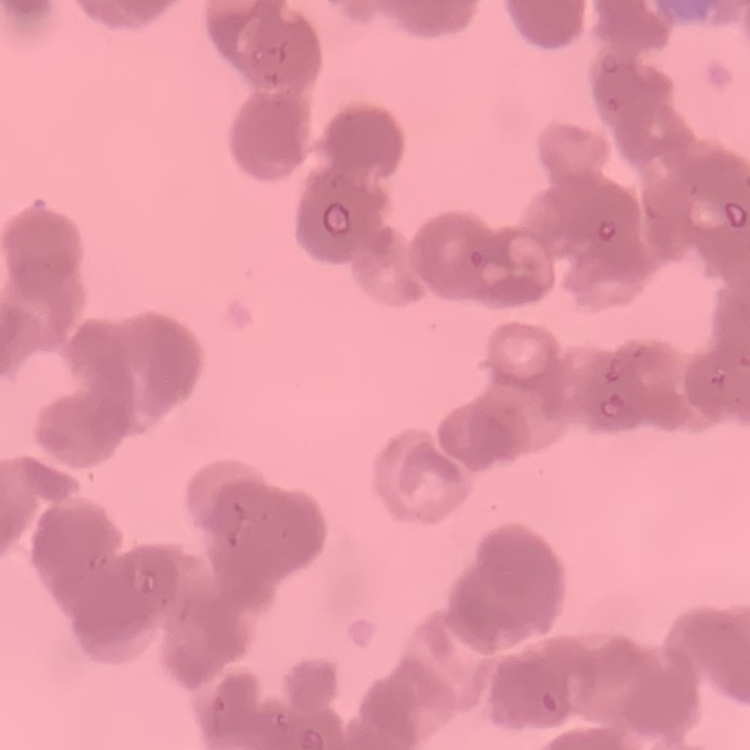
erythrocyte morphology = rouleaux formation
preparation = thin blood smear
image type = square crop of a larger photomicrograph
stain = Field's or Giemsa